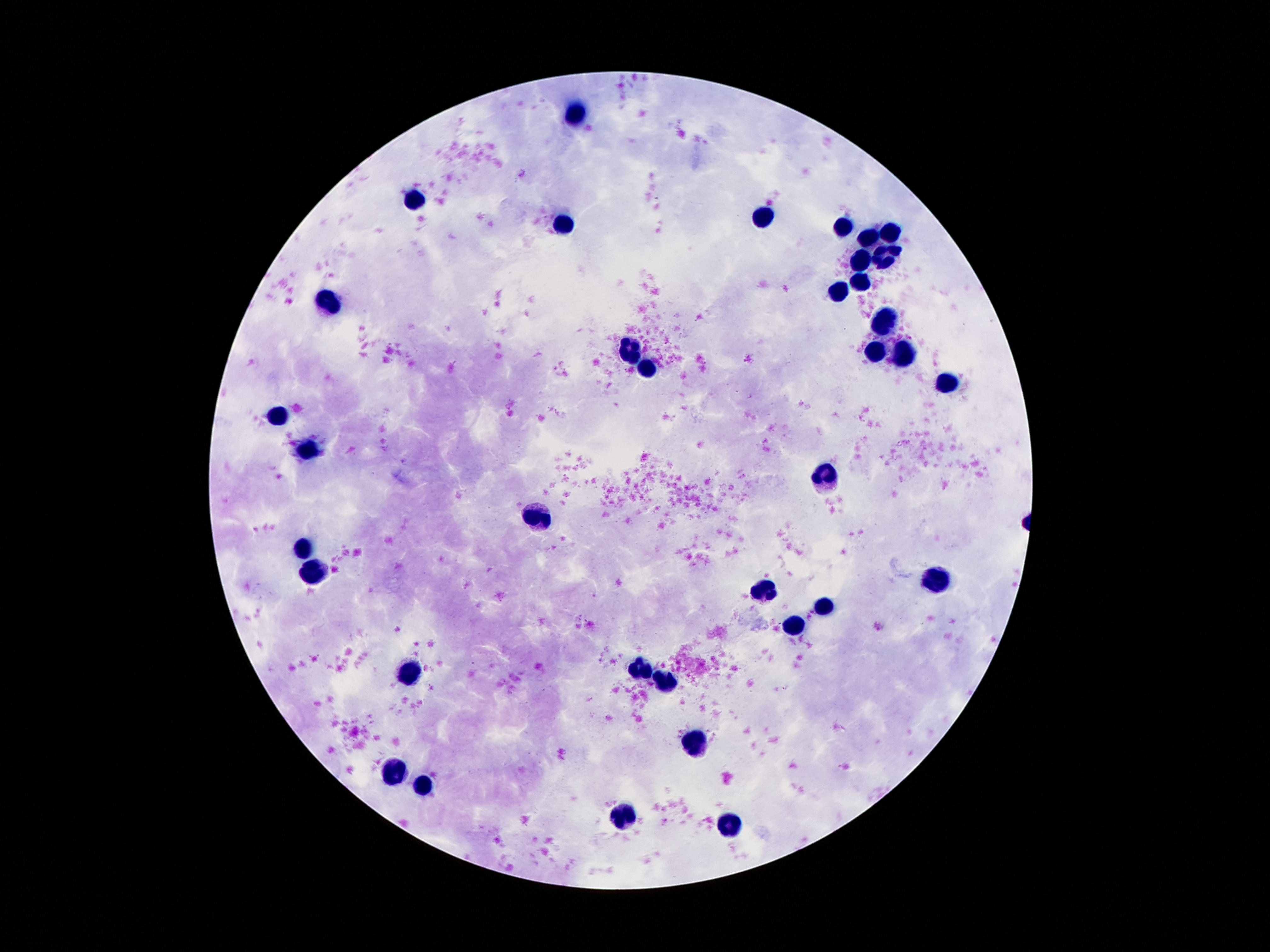
patient malaria status = not infected
field of view = single
image size = 1270×952 pixels
leukocyte locations = approximate centers as [x, y] in pixels: [578, 113], [417, 199], [766, 216], [563, 226], [843, 228], [889, 233], [871, 242], [886, 255], [858, 263], [861, 283], [837, 294], [324, 304], [889, 319], [628, 354], [910, 354], [871, 355], [645, 371], [951, 383], [277, 416], [307, 450], [826, 472], [535, 518], [305, 548], [313, 571], [938, 582], [766, 595], [820, 608], [792, 627], [410, 670], [639, 671], [664, 680], [697, 739], [393, 771], [421, 790], [623, 818], [729, 824]
capture = smartphone camera through the microscope eyepiece
preparation = thick blood film
stain = Giemsa
magnification = 100x